Report the malaria status of this cell.
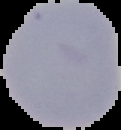

Uninfected.

Summary:
  - Image size: 121×130 pixels
  - Preparation: thin blood film
  - Image type: segmented cell region with the area outside set to black